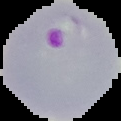
Summary:
  - Image size: 121×121 pixels
  - Preparation: thin blood smear
  - Image type: segmented cell region with the area outside set to black
  - Malaria status: parasitized